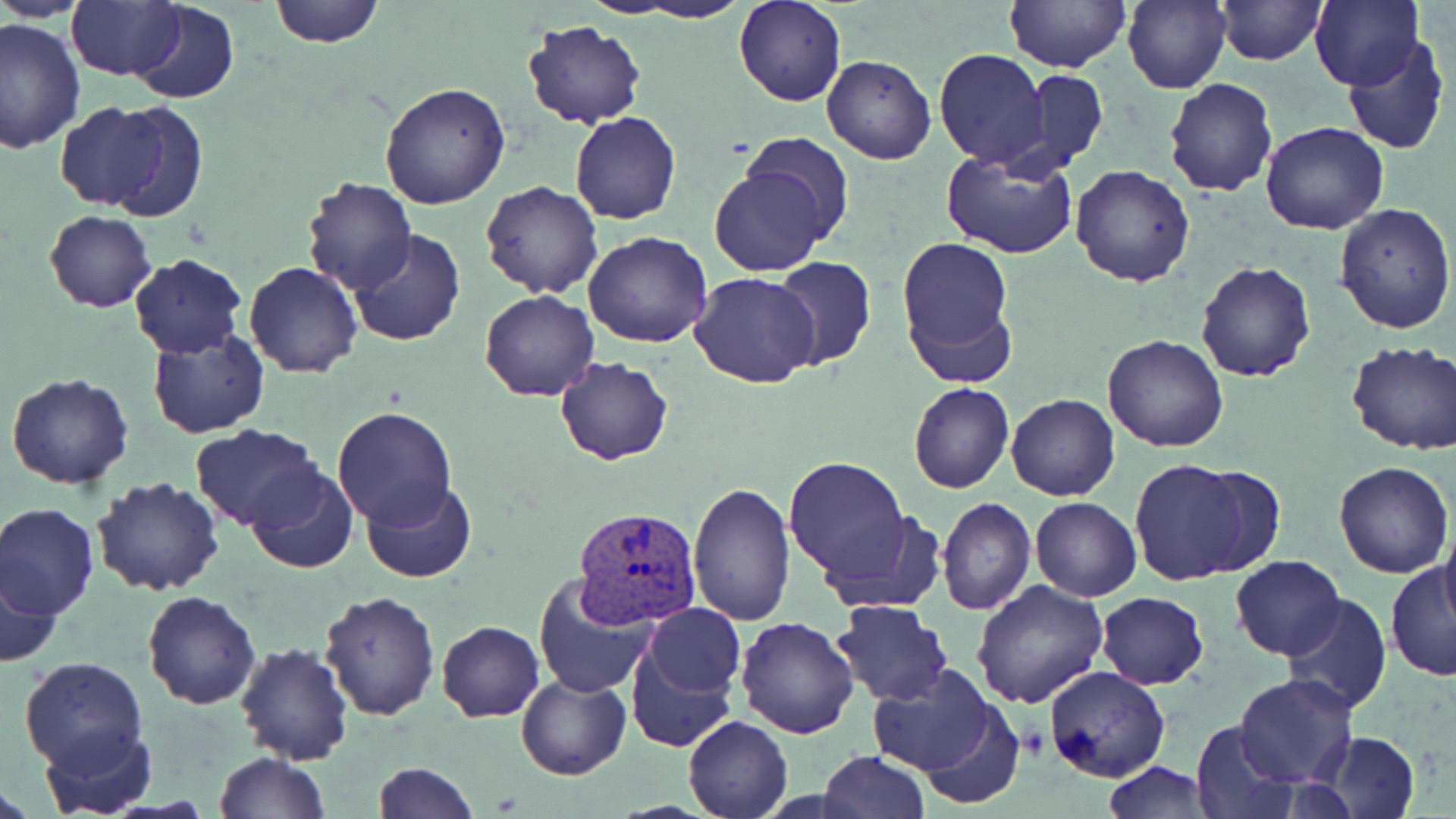

slide-level diagnosis = Plasmodium vivax
field of view = single
modality = optical microscopy
image size = 1456×819 pixels
uninfected red blood cell locations = approximate bounding boxes as (x1, y1, x2, y2) in pixels: (3, 0, 94, 21), (67, 0, 183, 81), (269, 0, 383, 47), (616, 0, 754, 23), (733, 0, 847, 108), (1003, 0, 1129, 72), (1123, 0, 1230, 94), (1215, 0, 1324, 65), (1310, 0, 1423, 91), (10, 1, 173, 120), (130, 1, 239, 105), (0, 17, 84, 154), (522, 20, 648, 130), (1341, 35, 1451, 156), (934, 48, 1049, 168), (822, 54, 936, 164), (1016, 71, 1107, 176), (1163, 76, 1278, 199), (380, 82, 511, 212), (50, 103, 178, 212), (570, 112, 681, 225), (1261, 122, 1390, 235), (738, 133, 856, 249), (942, 148, 1079, 260), (707, 163, 832, 278), (1070, 164, 1195, 286), (300, 177, 416, 296), (479, 181, 603, 299), (1334, 203, 1455, 335), (44, 209, 155, 312), (347, 231, 467, 348), (582, 231, 713, 349), (896, 235, 1015, 375), (129, 253, 247, 358), (770, 256, 877, 370), (1195, 260, 1317, 384), (243, 261, 363, 379), (689, 272, 821, 388), (480, 289, 600, 400), (147, 329, 269, 437), (1102, 333, 1228, 453), (1345, 341, 1456, 455), (554, 357, 672, 466), (6, 373, 134, 490), (908, 383, 1013, 495), (1007, 393, 1120, 503), (331, 407, 458, 528), (190, 423, 323, 532), (783, 456, 916, 585), (1130, 458, 1256, 587), (1333, 462, 1453, 580), (246, 464, 358, 572), (1188, 467, 1286, 574), (92, 477, 223, 596), (360, 479, 476, 583), (687, 480, 794, 624), (936, 497, 1036, 615), (1030, 497, 1142, 602), (0, 503, 100, 619), (820, 509, 944, 617), (1437, 513, 1456, 630), (1230, 555, 1346, 660), (1386, 560, 1456, 681), (2, 562, 67, 668), (532, 573, 658, 698), (971, 579, 1108, 708), (318, 589, 439, 722), (143, 590, 263, 710), (1094, 592, 1209, 688), (1282, 594, 1392, 713), (832, 600, 954, 705), (623, 612, 744, 754), (733, 616, 859, 738), (436, 619, 545, 722), (234, 643, 354, 764), (1269, 646, 1390, 778), (18, 657, 147, 774), (865, 665, 1002, 775), (1043, 668, 1169, 783), (516, 674, 630, 781), (1235, 674, 1358, 787), (910, 694, 1025, 807), (683, 714, 793, 818), (1189, 721, 1299, 817), (41, 725, 155, 816), (1314, 730, 1420, 818), (818, 751, 930, 819), (212, 752, 329, 819), (371, 761, 476, 819), (1102, 761, 1217, 817)
stain = May-Grünwald-Giemsa
Plasmodium vivax-infected red blood cell locations = approximate bounding boxes as (x1, y1, x2, y2) in pixels: (575, 505, 704, 628)
magnification = 1000x
preparation = thin blood film